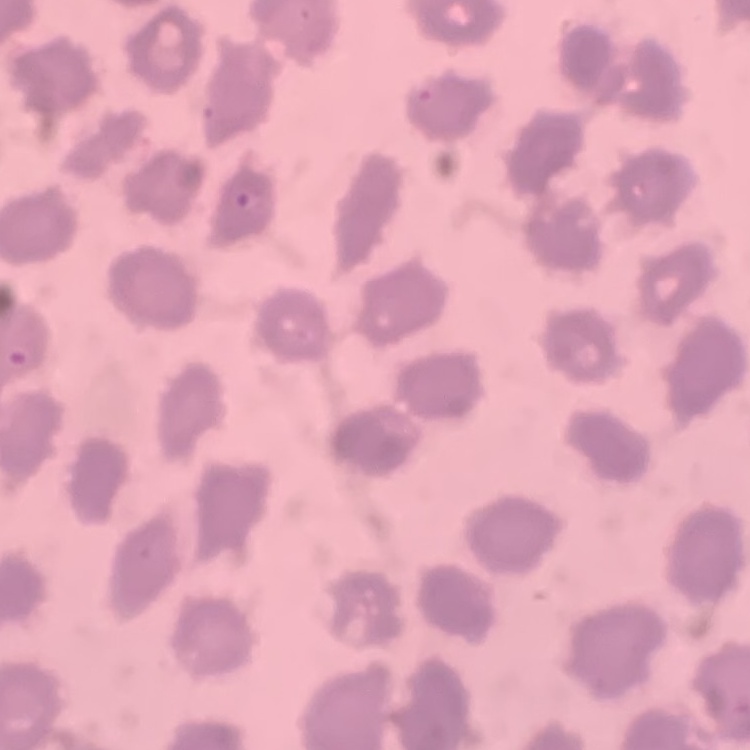

red blood cell morphology = no rouleaux formation
image type = one tile cut from a larger photomicrograph
preparation = thin blood film
stain = Field's or Giemsa